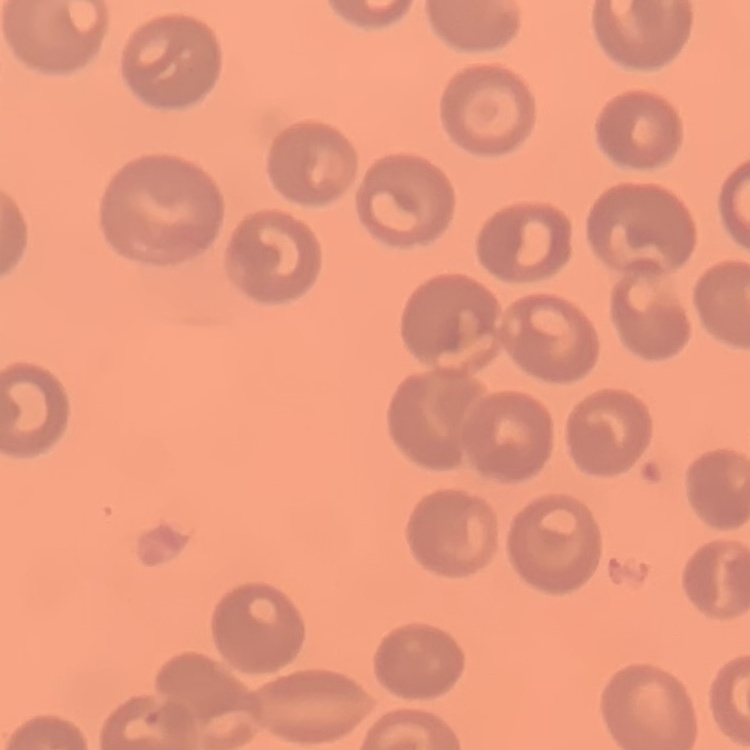
The erythrocytes exhibit no rouleaux formation. One tile cut from a larger photomicrograph. Thin blood film. Stained with either Field's or Giemsa.